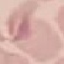

result: no malaria parasites seen
capture: smartphone through the microscope eyepiece
image_type: cell patch, automatically extracted from a larger field of view and resized to 64 × 64 pixels
stain: Giemsa
preparation: thin smear